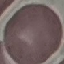
result = negative for malaria parasites
image type = cell patch, automatically extracted from a larger field of view and resized to 64 × 64 pixels
preparation = thin blood smear
stain = Giemsa
capture = smartphone camera at the microscope eyepiece